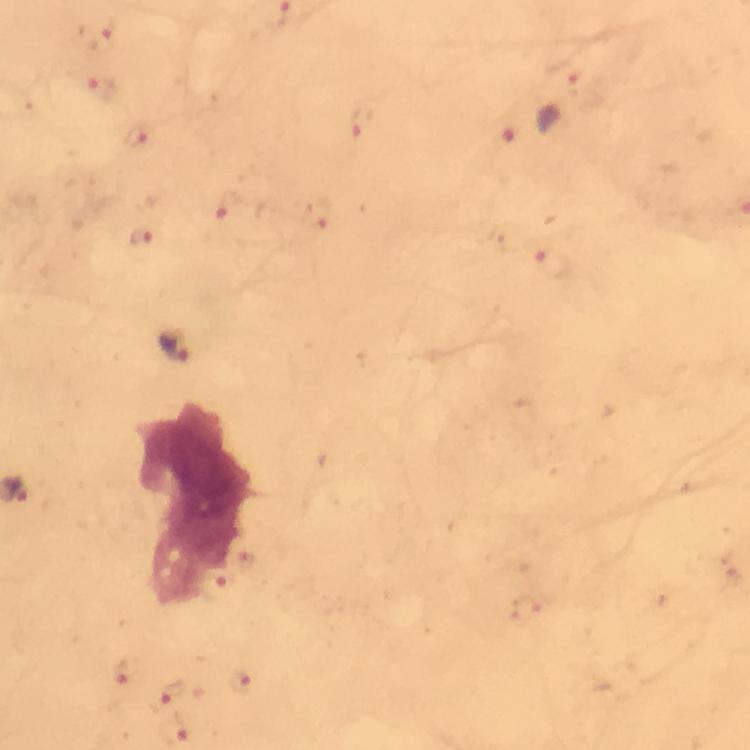
Approximate centers as (x, y) in pixels.
Summary:
  - Plasmodium parasite locations: (97, 36), (573, 81), (103, 89), (361, 122), (508, 131), (138, 137), (228, 204), (319, 217), (146, 237), (557, 260), (175, 345), (127, 670), (243, 676), (169, 698), (174, 729)
  - Preparation: thick smear
  - Cropped from: one field of view
  - Stain: Giemsa
  - Immersion oil: applied
  - Capture: smartphone camera through the microscope
  - Image size: 750×750 pixels
  - Context: from a malaria diagnostic workup
  - Magnification: 100x